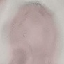

Summary:
  - Malaria status: uninfected
  - Capture: smartphone through the microscope eyepiece
  - Stain: Giemsa
  - Preparation: thin smear
  - Image type: cell patch, automatically extracted from a larger field of view and resized to 64 × 64 pixels